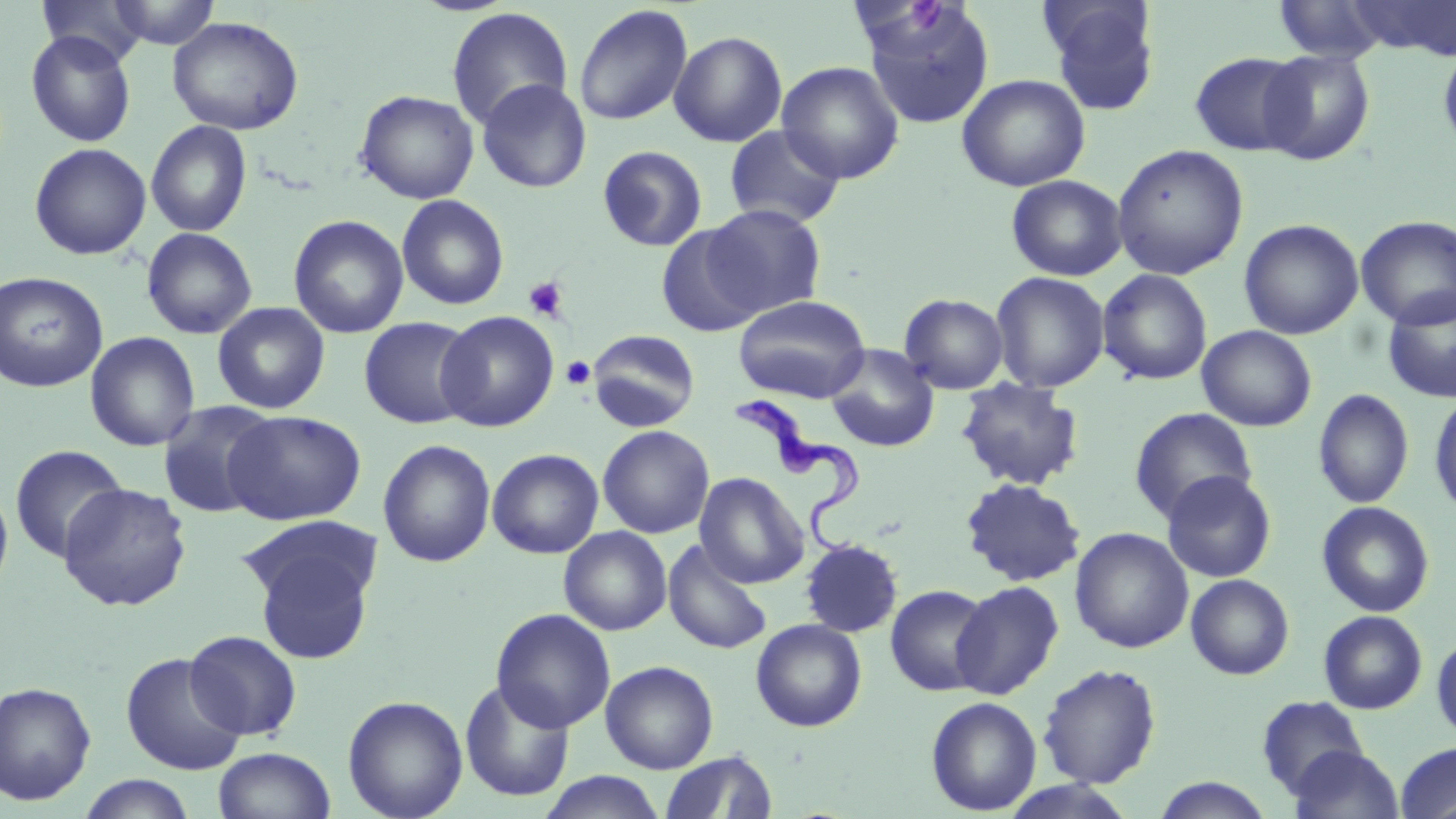
Summary:
  - Coordinate format: approximate bounding boxes as named x1/y1/x2/y2 corners in pixels
  - Uninfected red blood cell locations: (x1=37, y1=0, x2=150, y2=66), (x1=107, y1=0, x2=219, y2=49), (x1=1038, y1=0, x2=1161, y2=115), (x1=1272, y1=0, x2=1392, y2=63), (x1=1353, y1=1, x2=1455, y2=58), (x1=858, y1=2, x2=996, y2=128), (x1=573, y1=4, x2=693, y2=126), (x1=446, y1=7, x2=573, y2=130), (x1=167, y1=16, x2=304, y2=136), (x1=25, y1=29, x2=137, y2=148), (x1=669, y1=30, x2=788, y2=147), (x1=1438, y1=41, x2=1456, y2=158), (x1=1256, y1=48, x2=1375, y2=165), (x1=1189, y1=51, x2=1309, y2=157), (x1=776, y1=60, x2=906, y2=184), (x1=956, y1=73, x2=1090, y2=192), (x1=476, y1=79, x2=592, y2=193), (x1=355, y1=89, x2=479, y2=204), (x1=146, y1=120, x2=252, y2=237), (x1=724, y1=124, x2=846, y2=229), (x1=29, y1=142, x2=151, y2=260), (x1=1111, y1=144, x2=1249, y2=280), (x1=597, y1=145, x2=708, y2=252), (x1=1006, y1=175, x2=1128, y2=281), (x1=396, y1=194, x2=509, y2=310), (x1=703, y1=204, x2=828, y2=317), (x1=288, y1=214, x2=410, y2=339), (x1=1356, y1=215, x2=1456, y2=329), (x1=1239, y1=219, x2=1364, y2=340), (x1=655, y1=223, x2=766, y2=336), (x1=141, y1=227, x2=258, y2=339), (x1=1097, y1=268, x2=1213, y2=386), (x1=0, y1=271, x2=108, y2=392), (x1=990, y1=271, x2=1110, y2=392), (x1=1382, y1=290, x2=1456, y2=403), (x1=899, y1=293, x2=1008, y2=395), (x1=733, y1=295, x2=871, y2=403), (x1=212, y1=302, x2=330, y2=414), (x1=436, y1=311, x2=559, y2=432), (x1=358, y1=317, x2=477, y2=429), (x1=1196, y1=325, x2=1317, y2=431), (x1=586, y1=329, x2=701, y2=432), (x1=85, y1=331, x2=201, y2=452), (x1=826, y1=344, x2=940, y2=451), (x1=955, y1=378, x2=1084, y2=491), (x1=1313, y1=389, x2=1414, y2=508), (x1=1428, y1=390, x2=1456, y2=518), (x1=157, y1=400, x2=280, y2=519), (x1=1129, y1=407, x2=1257, y2=523), (x1=223, y1=409, x2=366, y2=525), (x1=597, y1=424, x2=714, y2=538), (x1=377, y1=439, x2=496, y2=567), (x1=9, y1=444, x2=128, y2=564), (x1=486, y1=449, x2=604, y2=559), (x1=1160, y1=470, x2=1277, y2=583), (x1=695, y1=472, x2=809, y2=588), (x1=0, y1=477, x2=14, y2=602), (x1=960, y1=478, x2=1087, y2=587), (x1=57, y1=482, x2=193, y2=612), (x1=1316, y1=501, x2=1435, y2=617), (x1=558, y1=526, x2=672, y2=635), (x1=1069, y1=527, x2=1194, y2=653), (x1=244, y1=536, x2=379, y2=664), (x1=662, y1=539, x2=773, y2=655), (x1=799, y1=539, x2=903, y2=638), (x1=1185, y1=573, x2=1294, y2=680), (x1=951, y1=580, x2=1063, y2=699), (x1=885, y1=584, x2=993, y2=697), (x1=490, y1=608, x2=616, y2=733), (x1=1318, y1=610, x2=1427, y2=714), (x1=750, y1=618, x2=867, y2=732), (x1=184, y1=630, x2=302, y2=740), (x1=1432, y1=634, x2=1456, y2=741), (x1=121, y1=652, x2=247, y2=777), (x1=600, y1=660, x2=719, y2=773), (x1=1037, y1=663, x2=1162, y2=788), (x1=459, y1=678, x2=575, y2=802), (x1=0, y1=681, x2=97, y2=805), (x1=342, y1=695, x2=468, y2=819), (x1=1256, y1=696, x2=1368, y2=799), (x1=925, y1=697, x2=1042, y2=815), (x1=1395, y1=742, x2=1456, y2=818), (x1=1288, y1=745, x2=1404, y2=819), (x1=212, y1=747, x2=336, y2=819), (x1=660, y1=750, x2=777, y2=819), (x1=537, y1=771, x2=667, y2=818), (x1=76, y1=775, x2=198, y2=818), (x1=1151, y1=777, x2=1276, y2=818)
  - Platelet locations: (x1=908, y1=1, x2=948, y2=31), (x1=523, y1=276, x2=568, y2=322), (x1=561, y1=355, x2=595, y2=389)
  - Trypanosoma brucei locations: (x1=733, y1=391, x2=866, y2=558)
  - Slide-level diagnosis: Trypanosoma brucei
  - Preparation: thin blood film
  - Field of view: single
  - Stain: May-Grünwald-Giemsa
  - Modality: light microscopy
  - Magnification: 1000x
  - Image size: 1456×819 pixels